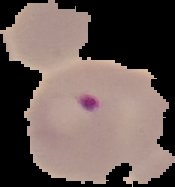 Image is 175×187 pixels. Segmented cell region on a black background. Result: Plasmodium parasites identified. From a thin blood film.